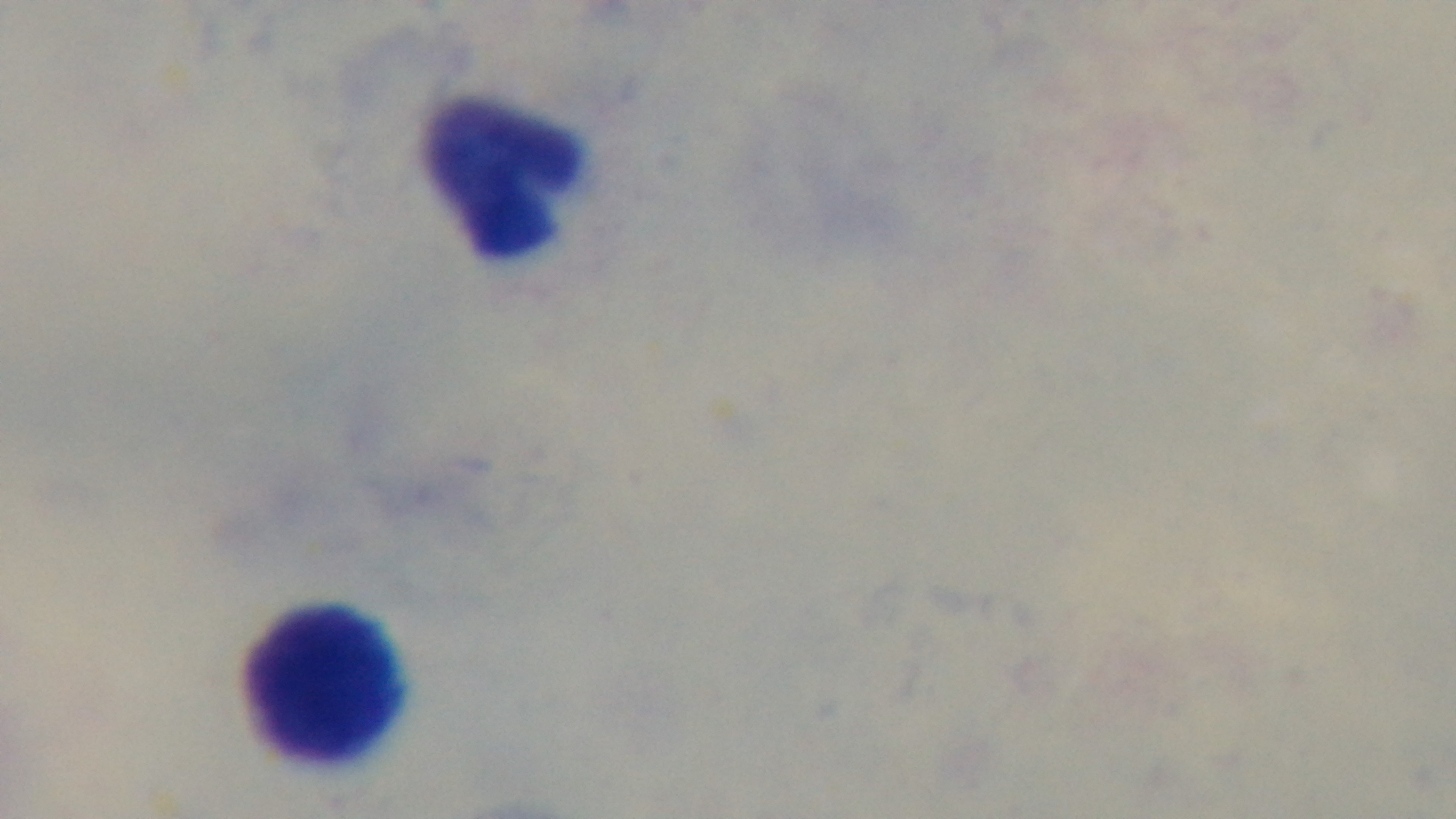
preparation = thick
modality = light microscopy
malaria status = negative
capture = mounted 4K digital camera
field of view = one from the slide
objective = 100x oil immersion
stain = Giemsa